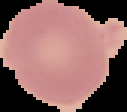
Summary:
  - Result: no Plasmodium parasites seen
  - Image size: 127×112 pixels
  - Image type: segmented cell region with the area outside set to black
  - Preparation: thin blood film